Classify this cell by malaria status.
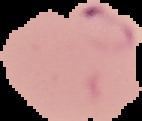

Parasitized.

Image is 142×121 pixels. Cell region segmented out of the field of view; the surrounding area is masked to black. From a thin blood smear.